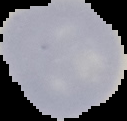
Segmented cell region on a black background. Result: no malaria parasites detected. Image is 127×121 pixels. From a thin blood film.